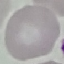

Malaria status: uninfected. Giemsa stain. Cell patch, automatically extracted from a larger field of view and resized to 64 × 64 pixels. Acquired by smartphone through the microscope eyepiece. Thin blood film.